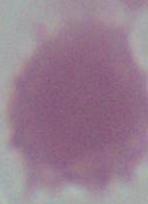

Summary:
  - Modality: micrograph
  - Magnification: 1000x
  - Identification: red blood cell